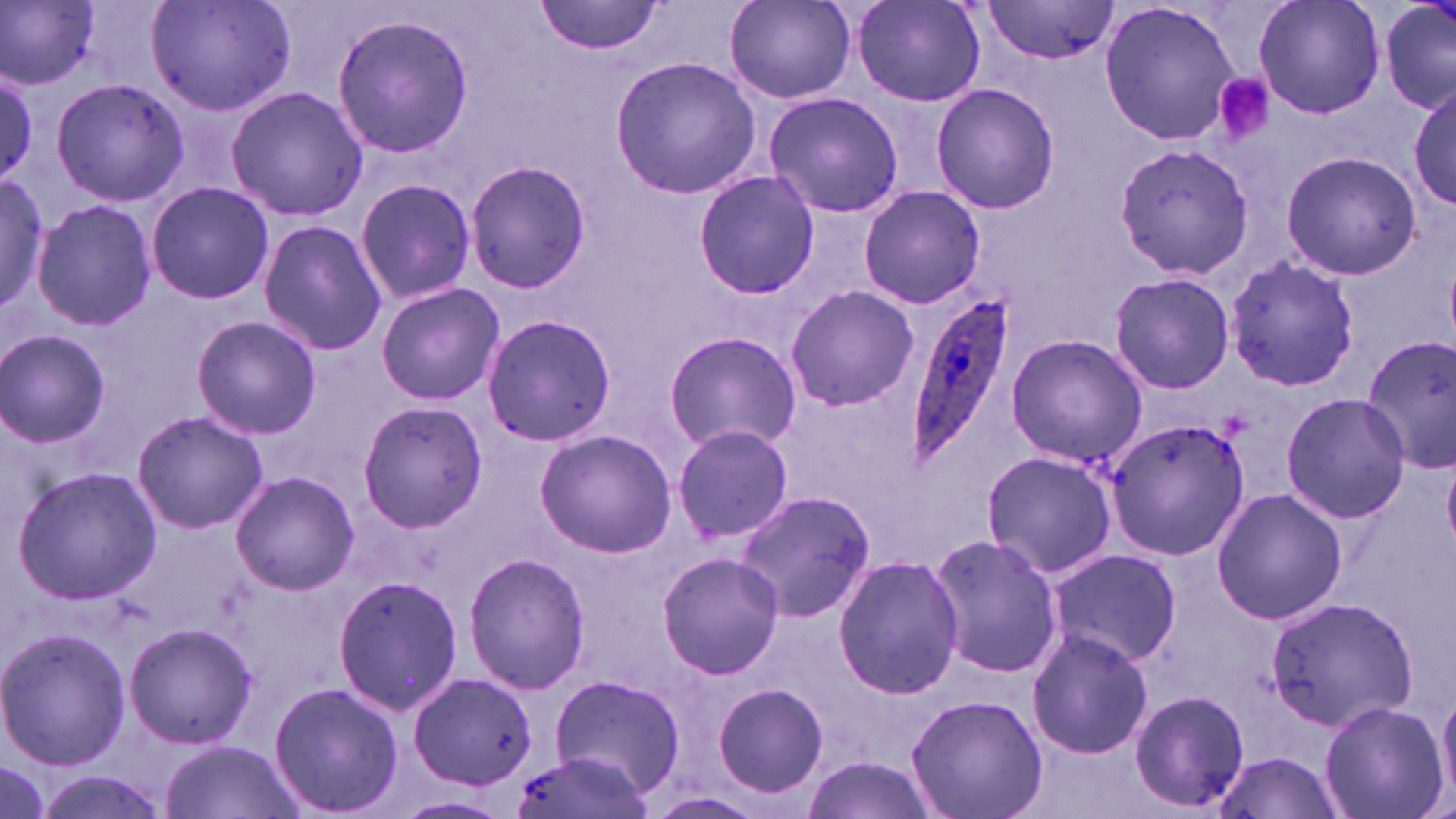
Summary:
  - Coordinate format: approximate bounding boxes as (x1, y1, x2, y2) in pixels
  - Plasmodium ovale-infected red blood cell locations: (905, 285, 1019, 468)
  - Uninfected red blood cell locations: (147, 0, 297, 117), (536, 0, 664, 55), (981, 0, 1113, 66), (1099, 0, 1246, 148), (1251, 0, 1387, 120), (1378, 0, 1456, 118), (2, 1, 101, 89), (725, 2, 856, 104), (852, 2, 985, 106), (332, 12, 474, 160), (611, 56, 761, 199), (2, 70, 40, 183), (50, 78, 189, 209), (1409, 81, 1456, 211), (930, 82, 1061, 213), (225, 86, 370, 220), (762, 91, 904, 216), (1113, 141, 1254, 281), (1281, 149, 1425, 281), (465, 160, 590, 294), (693, 170, 820, 298), (0, 172, 49, 314), (355, 178, 476, 305), (147, 180, 272, 305), (858, 186, 986, 311), (34, 200, 156, 330), (258, 219, 386, 355), (1224, 254, 1360, 395), (1108, 273, 1236, 394), (375, 282, 506, 406), (784, 284, 918, 413), (191, 315, 322, 440), (481, 315, 617, 447), (0, 328, 112, 448), (664, 331, 801, 453), (1005, 334, 1147, 468), (1361, 334, 1456, 471), (1281, 390, 1411, 523), (355, 402, 491, 534), (131, 410, 269, 535), (1104, 416, 1250, 562), (671, 425, 794, 544), (534, 429, 675, 556), (980, 450, 1117, 578), (1444, 457, 1456, 552), (12, 465, 161, 605), (229, 470, 360, 595), (734, 488, 877, 622), (1211, 488, 1347, 625), (927, 532, 1065, 679), (1045, 547, 1183, 666), (657, 551, 782, 680), (464, 552, 590, 696), (832, 556, 964, 700), (332, 572, 464, 717), (1264, 596, 1418, 735), (123, 622, 259, 751), (1027, 627, 1153, 759), (0, 629, 130, 769), (410, 672, 538, 790), (548, 673, 685, 793), (268, 681, 405, 818), (711, 681, 831, 800), (1436, 682, 1456, 807), (1129, 689, 1251, 812), (905, 694, 1048, 819), (1319, 700, 1447, 819), (162, 739, 302, 819), (507, 752, 652, 819), (1210, 752, 1346, 819), (798, 754, 937, 819), (28, 770, 167, 819), (645, 791, 769, 819)
  - Platelet locations: (1213, 75, 1273, 143)
  - Slide-level diagnosis: Plasmodium ovale
  - Magnification: 1000x
  - Image size: 1456×819 pixels
  - Modality: optical microscopy
  - Stain: May-Grünwald-Giemsa
  - Preparation: thin blood film
  - Field of view: one of a larger specimen